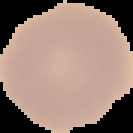

image size = 133×133 pixels
preparation = thin blood smear
image type = cell region segmented out of the field of view; surrounding area masked to black
malaria status = uninfected